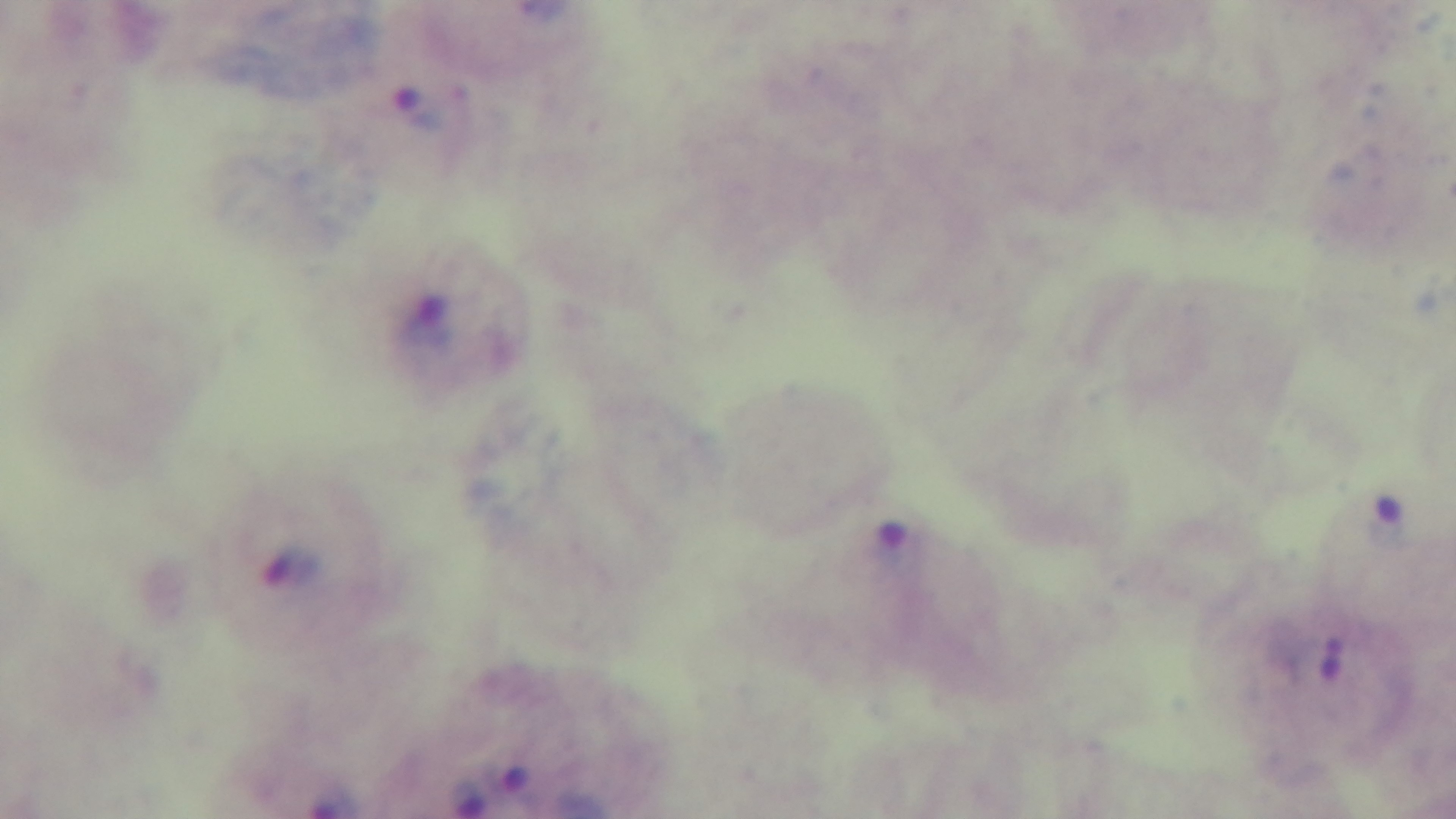

Summary:
  - Preparation: thick smear
  - Modality: light microscopy
  - Objective: 100x oil immersion
  - Malaria status: positive
  - Capture: mounted 4K digital camera
  - Field of view: one from the slide
  - Stain: Giemsa